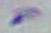

modality = micrograph
identification = Toxoplasma gondii
magnification = 1000x